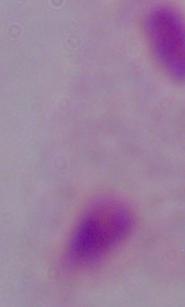
identification = trichomonad
magnification = 1000x
modality = photomicrograph